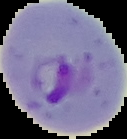 From a thin blood film. Segmented cell region on a black background. Image is 127×139 pixels. Result: Plasmodium parasites detected.